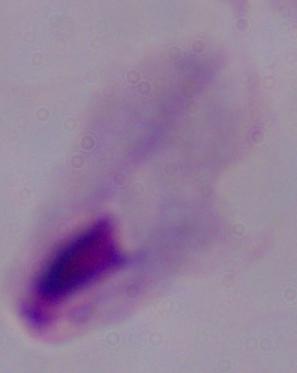

A trichomonad is shown. Captured at 1000x magnification. Micrograph.